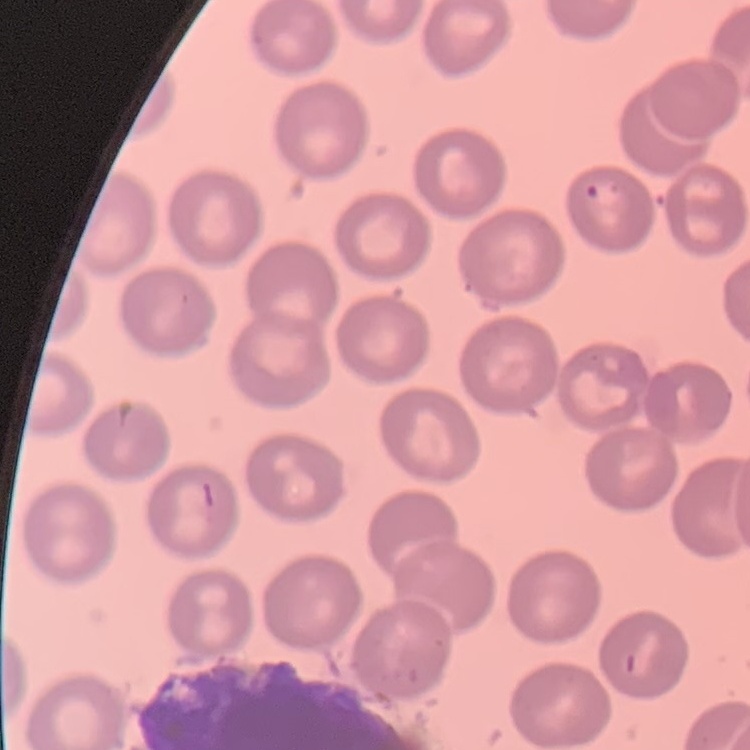

red_blood_cell_morphology: no rouleaux formation
image_type: one tile cut from a larger photomicrograph
stain: Field's or Giemsa
preparation: thin blood film